Identify the parasite.
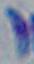
This is Toxoplasma gondii.

{
  "magnification": "1000x",
  "modality": "photomicrograph"
}